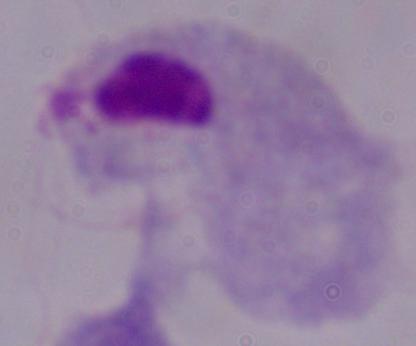 1000x magnification. A trichomonad is shown. Photomicrograph.